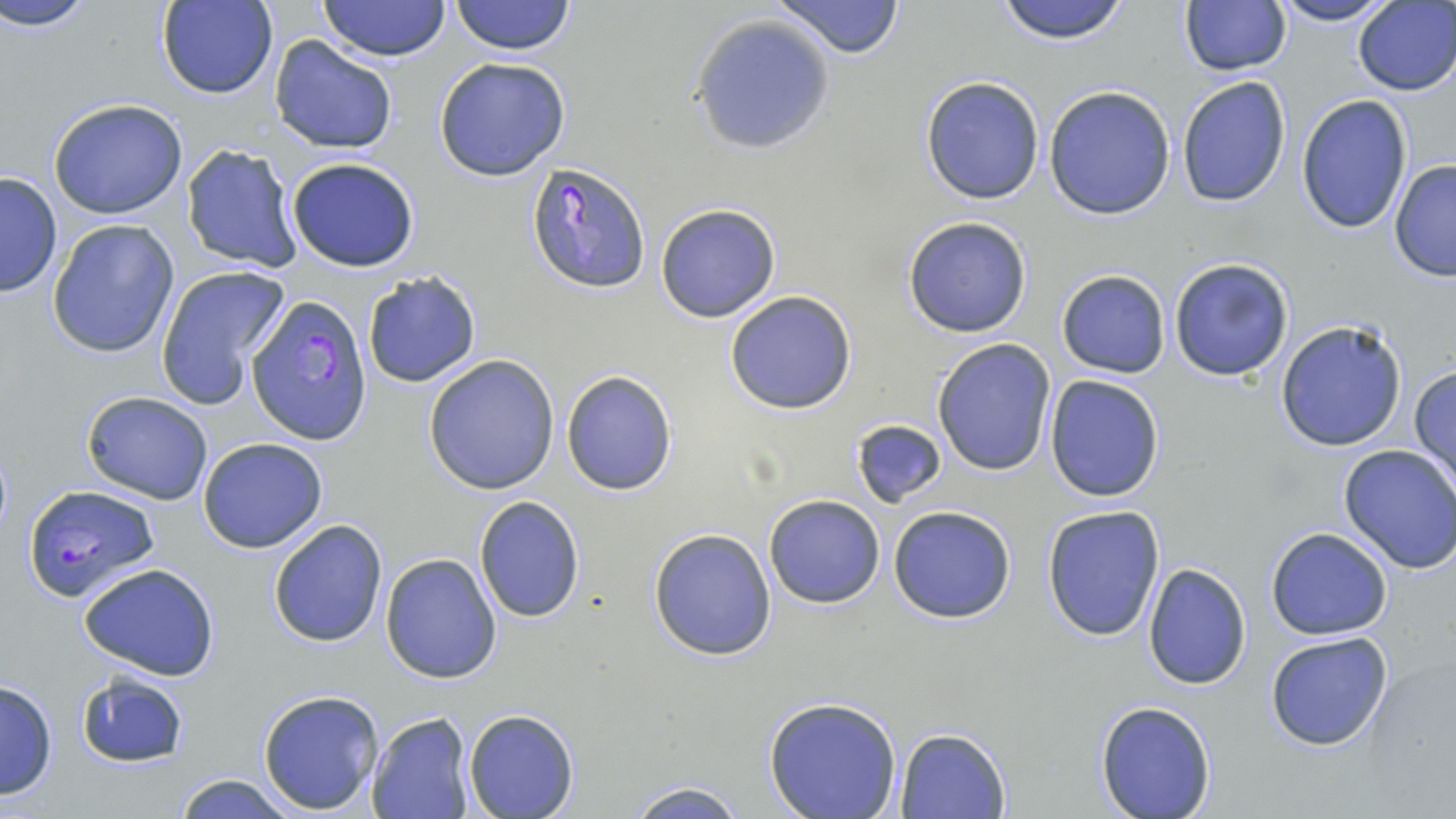
Approximate bounding boxes as (x1,y1)-(x2,y2) corner pairs in pixels. Plasmodium falciparum-infected red blood cell locations: (525,162)-(655,292), (246,295)-(372,445), (22,484)-(159,603). Uninfected red blood cell locations: (3,0)-(97,30), (449,0)-(575,55), (767,0)-(907,59), (991,0)-(1138,45), (1269,0)-(1398,26), (157,1)-(276,99), (318,1)-(452,61), (1179,1)-(1290,77), (1353,1)-(1455,96), (691,16)-(837,155), (269,36)-(399,156), (434,56)-(571,182), (919,75)-(1046,205), (1176,76)-(1290,208), (1043,86)-(1176,220), (1295,94)-(1413,235), (48,97)-(188,220), (182,144)-(304,274), (284,157)-(420,272), (1389,159)-(1456,283), (0,172)-(63,297), (656,203)-(781,323), (902,216)-(1032,338), (47,218)-(181,360), (1168,256)-(1296,383), (155,265)-(289,410), (1056,270)-(1171,378), (362,271)-(482,388), (724,290)-(856,414), (1274,318)-(1408,453), (931,338)-(1057,476), (423,354)-(559,495), (1409,364)-(1456,489), (561,369)-(678,497), (1044,375)-(1166,502), (80,390)-(212,504), (851,420)-(947,509), (198,437)-(328,553), (1337,445)-(1456,574), (474,495)-(586,623), (764,495)-(885,608), (888,505)-(1018,624), (1041,506)-(1165,642), (268,518)-(387,648), (648,527)-(777,661), (1266,528)-(1393,640), (380,553)-(503,684), (1142,563)-(1251,689), (78,564)-(221,681), (1265,632)-(1394,752), (75,673)-(189,768), (0,678)-(58,800), (257,687)-(384,814), (761,695)-(904,819), (1094,700)-(1218,818), (463,707)-(578,818), (368,711)-(475,819), (894,726)-(1010,817), (173,773)-(298,818), (622,778)-(752,818). Slide-level diagnosis: Plasmodium falciparum. One field of a larger specimen. Thin blood smear. Captured at 1000x magnification. Image is 1456×819 pixels. May-Grünwald-Giemsa-stained preparation. Optical microscopy.